Assess for Plasmodium parasites.
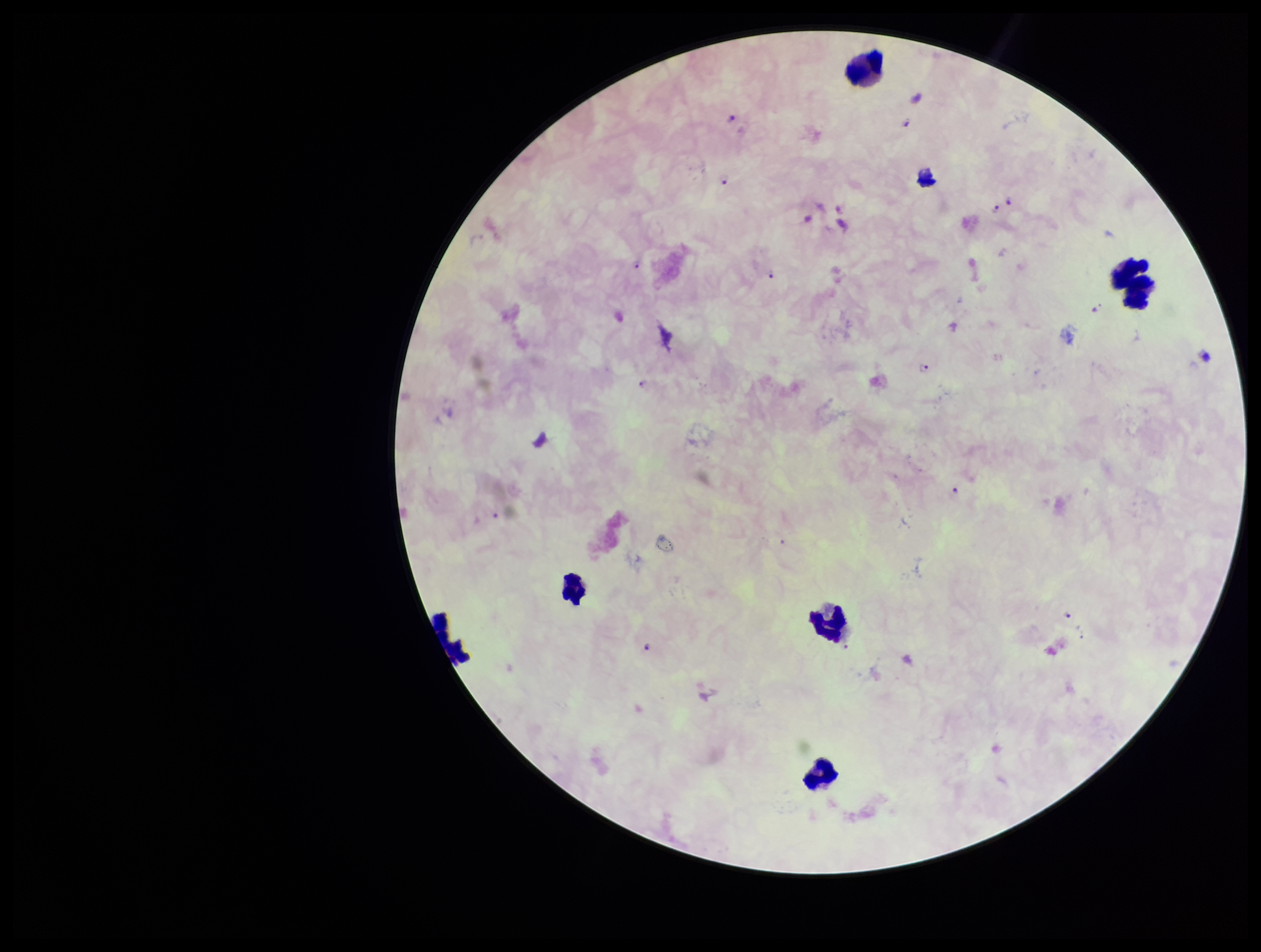
Identified.

{
  "leukocyte_count": 6,
  "image_size": "1261×952 pixels",
  "parasite_count": 13,
  "field_of_view": "single",
  "preparation": "thick blood smear",
  "species_reported_for_this_patient": "Plasmodium falciparum",
  "stain": "Giemsa",
  "capture": "smartphone photograph through the microscope eyepiece",
  "patient_malaria_status": "infected"
}